Classify the preparation.
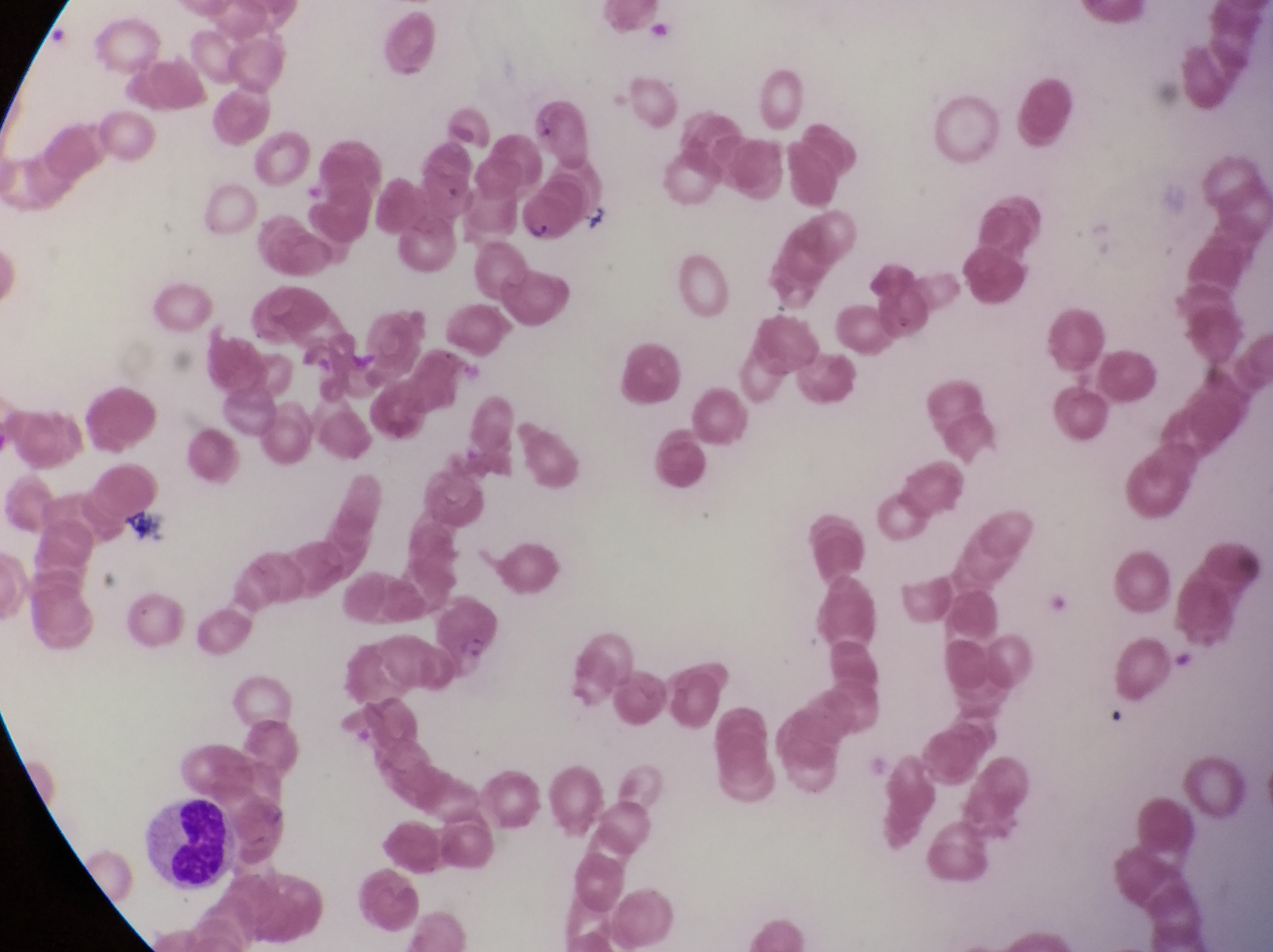
Thin blood smear.

Approximate bounding boxes as {left, top, right, bottom} in pixels. Leukocyte locations: {142, 797, 237, 890}. Parasitised red blood cell locations: {516, 185, 578, 245}. Image is 1273×952 pixels. One field of view. Captured by a smartphone held over the eyepiece of an Olympus CX-23 microscope. At a magnification of 1000x. Sample from Uganda.